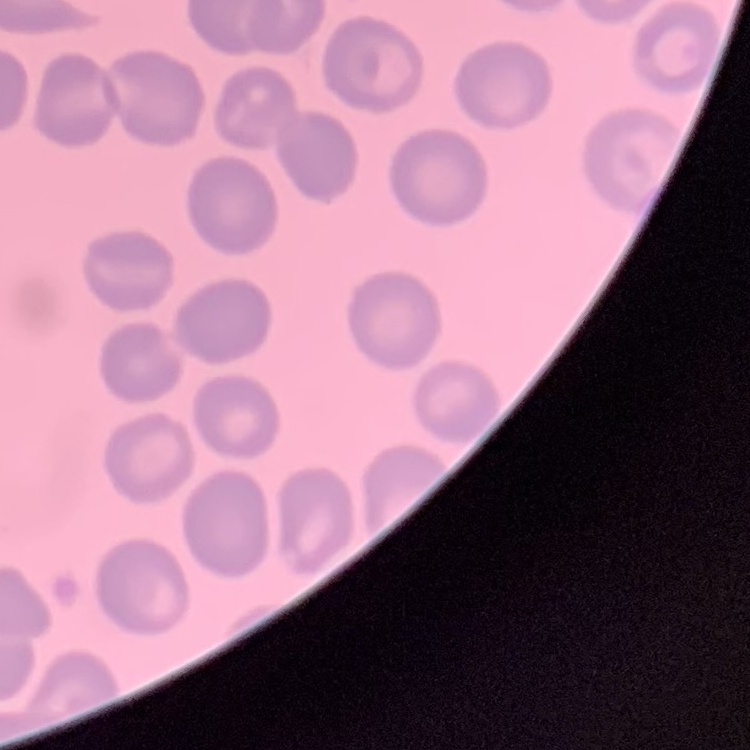
The erythrocytes exhibit no rouleaux formation. One tile cut from a larger photomicrograph. Thin blood smear. Stained with either Field's or Giemsa.